Identify the cell.
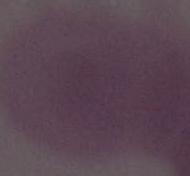
This is an erythrocyte.

modality = micrograph
magnification = 1000x